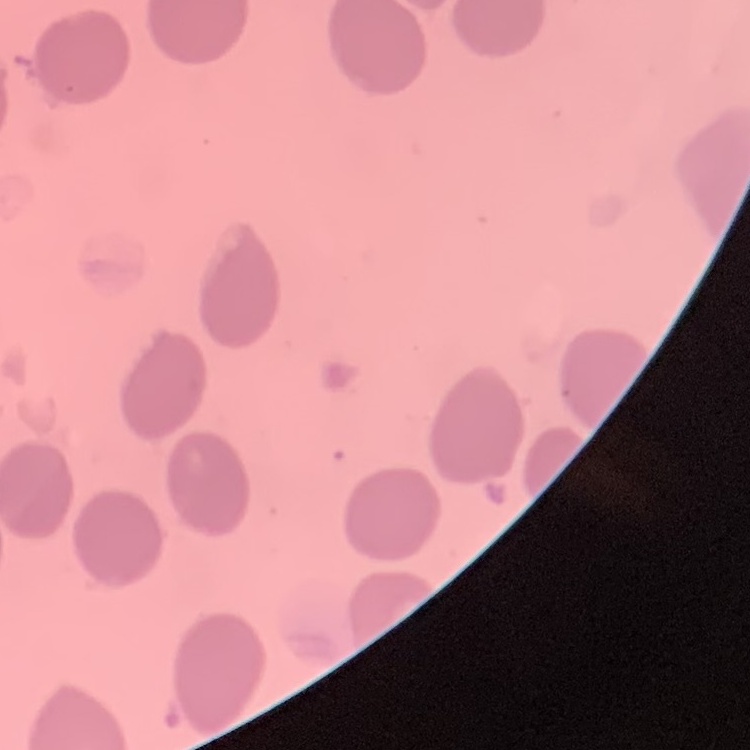
Summary:
  - Erythrocyte morphology: no rouleaux formation
  - Stain: Field's or Giemsa
  - Preparation: thin peripheral smear
  - Image type: one tile cut from a larger photomicrograph